Name the parasite shown.
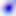

Toxoplasma gondii.

modality = micrograph
magnification = 400x